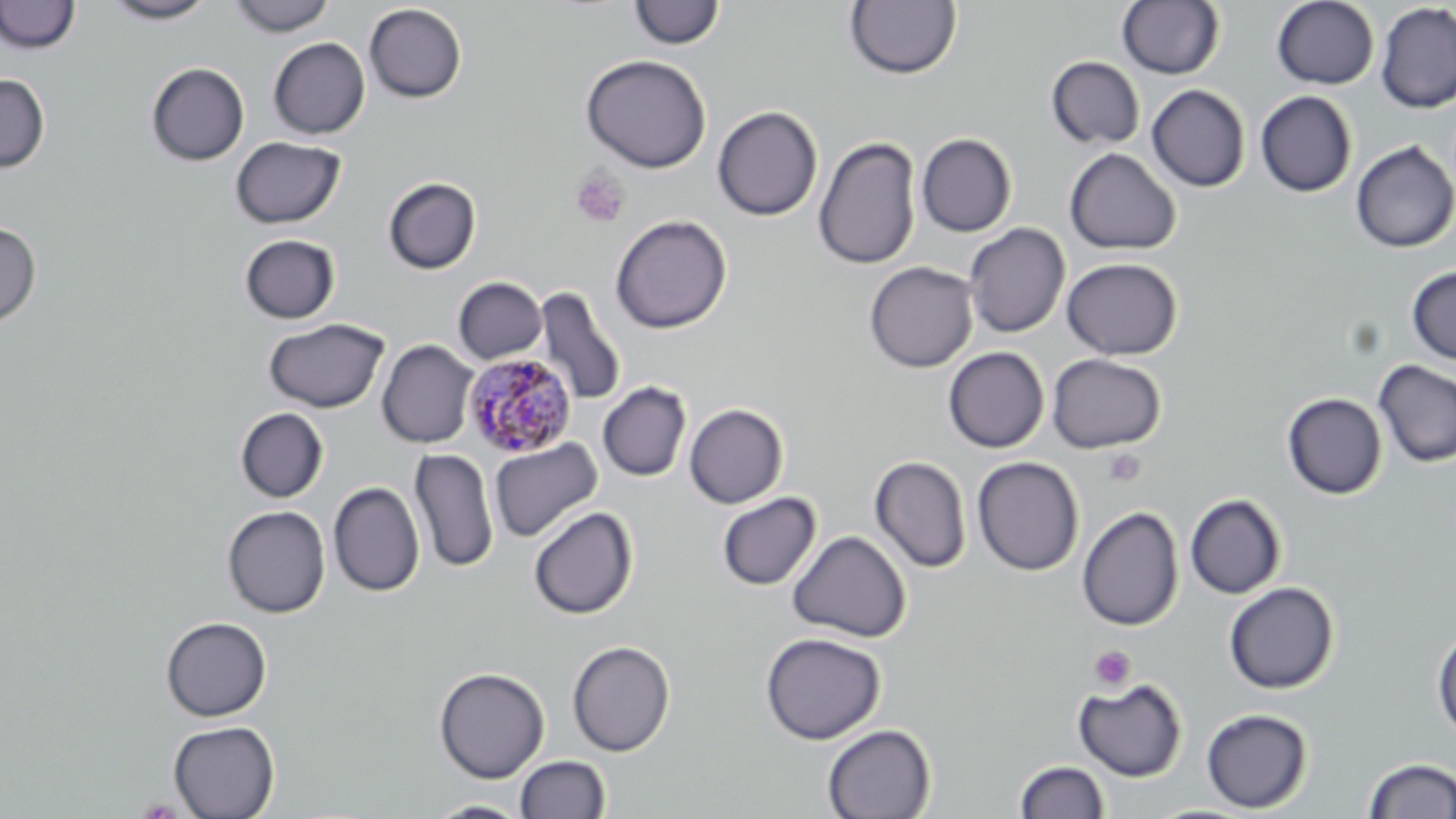

Approximate bounding boxes as [x1, y1, x2, y2] in pixels. Uninfected red blood cell locations: [0, 0, 81, 55], [103, 0, 218, 24], [228, 0, 337, 37], [1272, 0, 1380, 89], [629, 1, 725, 50], [845, 1, 961, 80], [1117, 1, 1226, 80], [363, 3, 467, 104], [1376, 3, 1456, 114], [268, 37, 370, 139], [580, 54, 711, 173], [1046, 57, 1145, 150], [146, 62, 249, 166], [0, 74, 50, 172], [1146, 85, 1251, 193], [1255, 90, 1358, 197], [712, 105, 823, 221], [916, 133, 1017, 237], [230, 136, 346, 229], [814, 136, 922, 271], [1351, 141, 1456, 253], [1065, 148, 1181, 255], [382, 176, 482, 275], [610, 214, 732, 334], [0, 222, 41, 327], [964, 223, 1070, 338], [239, 234, 341, 324], [1062, 257, 1183, 360], [864, 261, 978, 373], [1406, 265, 1456, 365], [453, 276, 547, 364], [533, 286, 627, 407], [264, 318, 389, 413], [377, 339, 479, 449], [943, 346, 1049, 453], [1047, 353, 1166, 453], [1373, 359, 1456, 468], [597, 381, 692, 482], [1282, 393, 1387, 499], [684, 403, 788, 509], [235, 408, 329, 503], [489, 438, 604, 543], [408, 448, 499, 574], [869, 456, 972, 574], [972, 456, 1085, 576], [328, 482, 425, 597], [716, 492, 821, 590], [1185, 494, 1287, 599], [222, 505, 331, 618], [528, 506, 638, 620], [1076, 506, 1184, 631], [787, 531, 911, 643], [1223, 582, 1339, 694], [161, 616, 272, 722], [1432, 629, 1456, 739], [760, 632, 885, 745], [567, 640, 675, 756], [434, 666, 550, 783], [1073, 678, 1188, 782], [1201, 708, 1313, 813], [168, 720, 280, 819], [822, 724, 937, 819], [515, 756, 611, 819], [1362, 757, 1456, 818], [1015, 760, 1110, 818], [424, 799, 532, 818]. Plasmodium malariae-infected red blood cell locations: [462, 353, 577, 458]. Platelet locations: [570, 169, 631, 228], [1102, 448, 1146, 487], [1089, 645, 1135, 690]. Slide-level diagnosis: Plasmodium malariae. Image is 1456×819 pixels. May-Grünwald-Giemsa stain. Single field of view. Light microscopy. 1000x magnification. Thin blood film.